Classify this cell by malaria status.
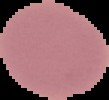

Uninfected.

Summary:
  - Image size: 109×100 pixels
  - Preparation: thin blood smear
  - Image type: segmented cell region with the area outside set to black